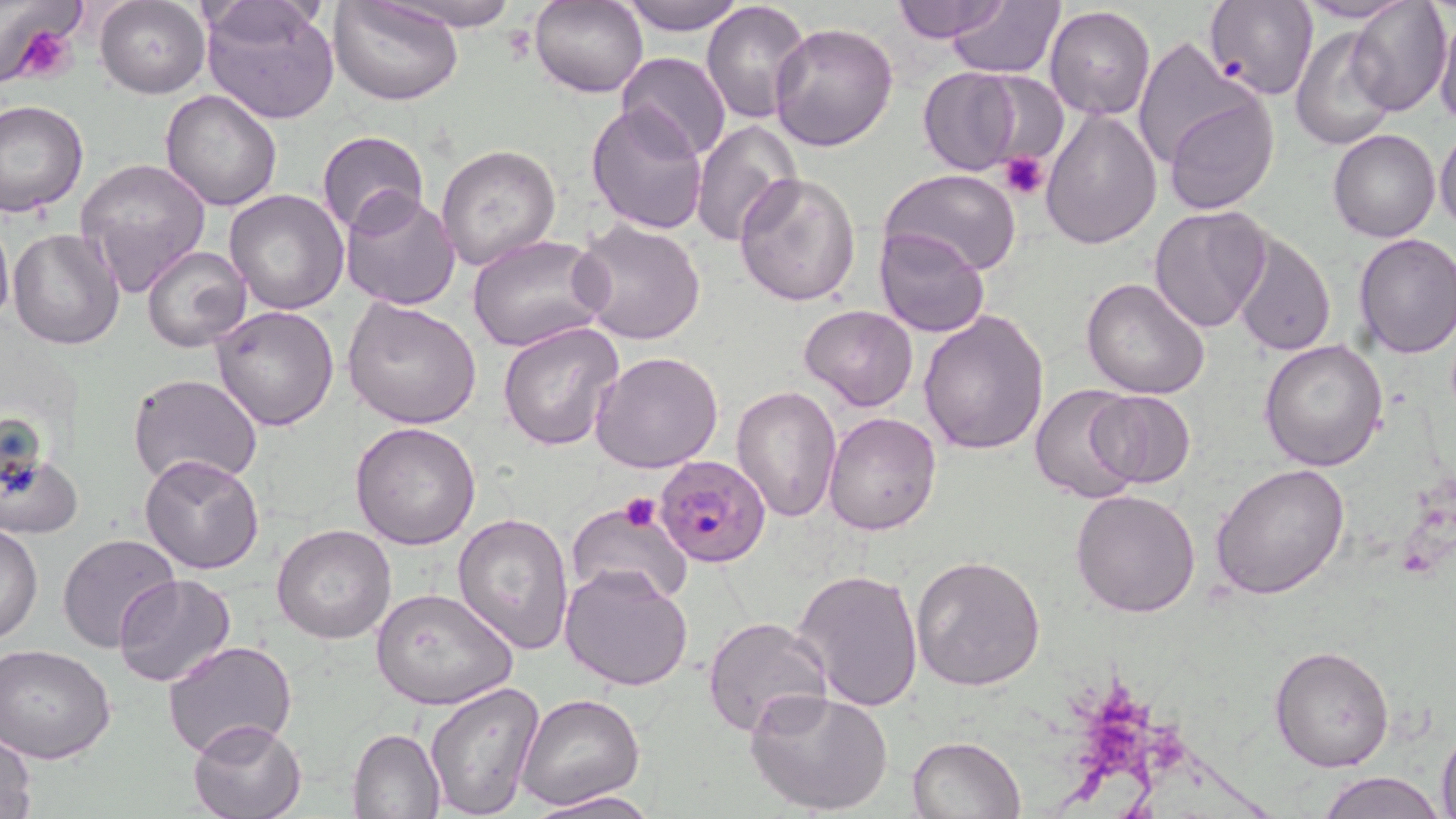

Approximate bounding boxes as [x1, y1, x2, y2] in pixels. Uninfected red blood cell locations: [374, 0, 525, 32], [619, 0, 748, 35], [700, 0, 812, 124], [890, 0, 1007, 43], [1348, 0, 1453, 115], [329, 1, 463, 106], [532, 1, 648, 99], [1205, 1, 1317, 100], [94, 2, 211, 98], [946, 2, 1064, 76], [1291, 2, 1417, 25], [201, 3, 342, 125], [1044, 5, 1155, 120], [1435, 13, 1456, 131], [768, 23, 898, 153], [1289, 27, 1398, 151], [1129, 35, 1268, 179], [616, 52, 732, 163], [918, 67, 1024, 175], [1157, 86, 1280, 215], [161, 88, 283, 211], [1, 100, 89, 218], [585, 102, 710, 233], [1040, 107, 1162, 250], [692, 118, 800, 249], [1435, 128, 1456, 229], [316, 129, 429, 236], [1328, 130, 1440, 243], [436, 143, 562, 271], [76, 158, 212, 293], [880, 169, 1021, 276], [732, 170, 861, 307], [224, 189, 349, 315], [339, 189, 460, 312], [1149, 205, 1272, 333], [0, 214, 13, 334], [573, 219, 706, 345], [8, 227, 125, 350], [873, 228, 990, 339], [1233, 233, 1336, 357], [1352, 234, 1456, 358], [467, 235, 610, 354], [140, 247, 252, 350], [1081, 277, 1211, 399], [343, 296, 481, 430], [211, 303, 341, 430], [799, 304, 918, 412], [918, 308, 1050, 455], [498, 319, 624, 452], [1259, 338, 1388, 470], [592, 350, 725, 474], [127, 373, 264, 492], [732, 384, 843, 522], [1030, 385, 1144, 505], [1084, 390, 1196, 489], [823, 413, 941, 534], [350, 421, 482, 551], [0, 445, 81, 541], [139, 454, 268, 574], [1211, 462, 1350, 599], [1071, 488, 1202, 617], [565, 501, 693, 606], [453, 512, 576, 653], [1, 522, 42, 646], [271, 524, 396, 643], [57, 534, 181, 653], [910, 554, 1046, 692], [560, 564, 695, 692], [791, 568, 924, 710], [114, 575, 236, 689], [371, 588, 518, 712], [702, 615, 833, 739], [163, 638, 298, 759], [1, 644, 116, 765], [1270, 644, 1396, 773], [425, 681, 544, 816], [745, 687, 894, 817], [514, 693, 644, 811], [188, 718, 308, 819], [1435, 721, 1456, 819], [347, 728, 445, 819], [1, 731, 38, 819], [907, 735, 1024, 818], [1318, 772, 1445, 819], [523, 788, 663, 819]. Plasmodium falciparum-infected red blood cell locations: [655, 454, 771, 567]. Platelet locations: [5, 21, 79, 85], [1000, 151, 1049, 201], [619, 493, 662, 533]. Slide-level diagnosis: Plasmodium falciparum. Optical microscopy. One field of a larger specimen. 1000x magnification. Image is 1456×819 pixels. May-Grünwald-Giemsa-stained preparation. Thin blood film.